Report the malaria status of this cell.
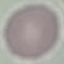

Uninfected.

Cell patch, automatically extracted from a larger field of view and resized to 64 × 64 pixels. Thin smear of blood. Photographed with a smartphone camera at the microscope eyepiece. Giemsa stain.